Assess this cell for malaria.
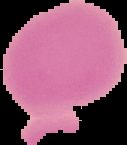

It is uninfected.

image size = 127×145 pixels
preparation = thin blood smear
image type = segmented cell region with the area outside set to black